Locate the P. falciparum-infected red blood cells and any of indeterminate infection status.
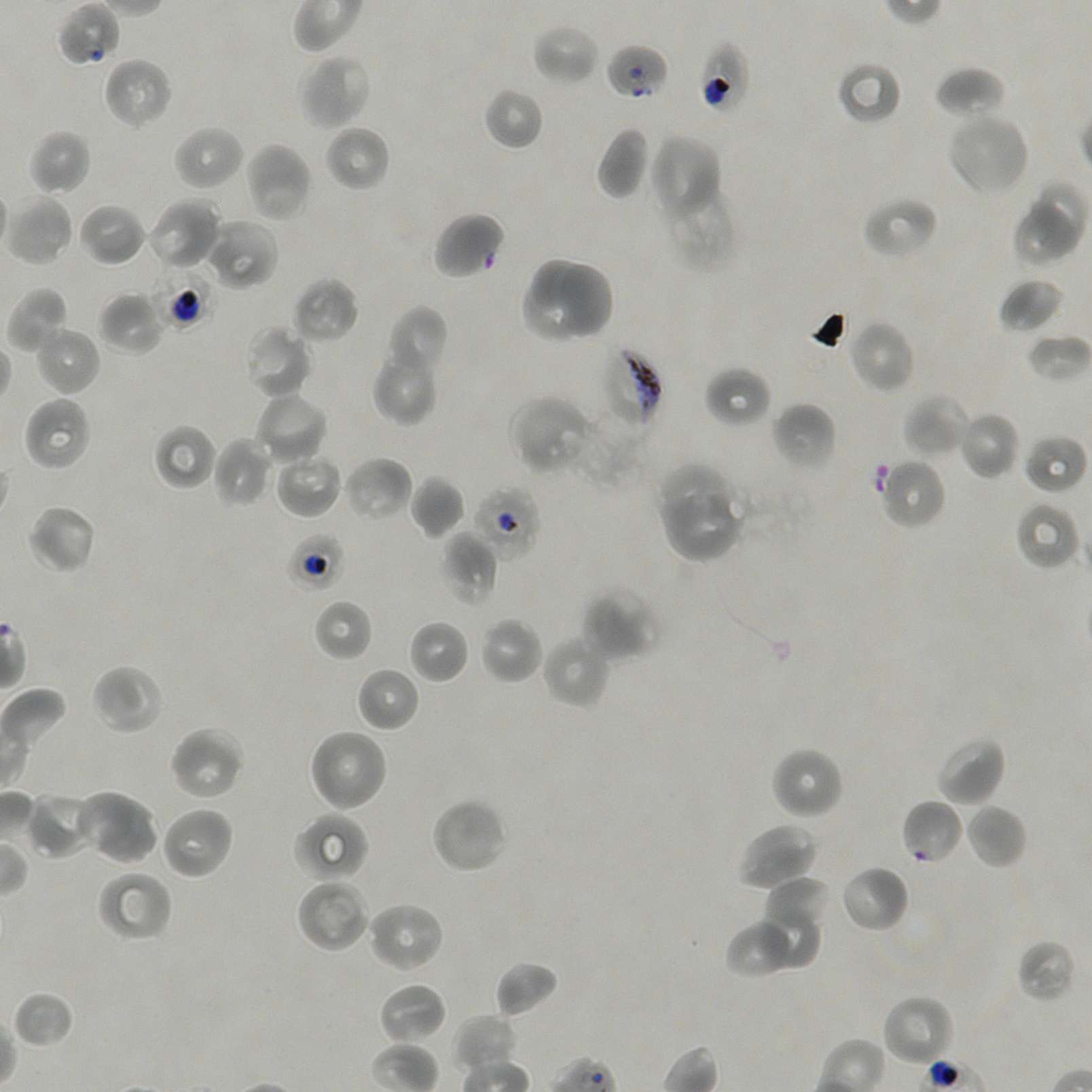

Approximate bounding boxes as {x1, y1, x2, y2} in pixels. Not every red blood cell is marked.
Infected red blood cells: {600, 347, 663, 431}.
Red blood cells of indeterminate infection status: {56, 1, 120, 67}, {697, 41, 751, 115}, {604, 44, 670, 101}, {431, 212, 507, 280}, {156, 267, 211, 328}, {470, 484, 543, 562}, {286, 533, 344, 593}, {901, 798, 964, 864}.

{
  "locations_of_uninfected_red_blood_cells": "{532, 24, 600, 86}, {299, 54, 372, 130}, {102, 57, 174, 130}, {835, 59, 903, 126}, {934, 67, 1006, 120}, {484, 86, 545, 150}, {945, 111, 1030, 197}, {172, 124, 245, 191}, {325, 125, 391, 192}, {596, 126, 650, 199}, {29, 130, 92, 196}, {649, 134, 722, 221}, {244, 141, 313, 223}, {662, 184, 739, 273}, {1025, 184, 1087, 255}, {5, 194, 75, 267}, {862, 195, 939, 260}, {147, 196, 223, 272}, {77, 202, 147, 267}, {1011, 206, 1073, 268}, {203, 218, 279, 291}, {560, 257, 614, 340}, {531, 259, 586, 310}, {291, 276, 359, 345}, {998, 277, 1064, 334}, {522, 282, 587, 341}, {5, 286, 70, 355}, {97, 291, 165, 356}, {386, 305, 449, 378}, {848, 319, 916, 393}, {33, 324, 101, 397}, {244, 324, 314, 401}, {1026, 332, 1091, 384}, {371, 346, 439, 426}, {704, 365, 771, 429}, {253, 390, 329, 465}, {904, 393, 971, 458}, {509, 394, 593, 475}, {22, 395, 93, 472}, {771, 401, 836, 472}, {568, 408, 647, 487}, {958, 410, 1021, 480}, {153, 424, 217, 491}, {1024, 433, 1087, 496}, {211, 437, 273, 509}, {272, 449, 343, 520}, {342, 455, 413, 523}, {878, 457, 947, 530}, {653, 463, 731, 532}, {408, 475, 465, 539}, {664, 494, 744, 562}, {1013, 501, 1081, 571}, {27, 503, 98, 575}, {441, 532, 498, 606}, {580, 585, 658, 662}, {312, 598, 374, 662}, {479, 616, 543, 685}, {407, 619, 470, 685}, {541, 633, 613, 709}, {90, 663, 165, 735}, {356, 667, 420, 733}, {168, 726, 247, 801}, {307, 728, 388, 812}, {934, 735, 1007, 807}, {769, 745, 845, 820}, {75, 788, 159, 866}, {28, 793, 98, 860}, {430, 797, 508, 875}, {965, 803, 1027, 869}, {160, 805, 234, 881}, {293, 812, 369, 881}, {737, 821, 820, 892}, {839, 864, 909, 933}, {96, 871, 172, 943}, {295, 877, 371, 953}, {763, 877, 833, 938}, {367, 901, 445, 973}, {755, 903, 817, 970}, {725, 918, 799, 979}, {1015, 939, 1077, 1004}, {494, 961, 560, 1018}, {378, 983, 448, 1045}, {12, 990, 75, 1049}, {881, 993, 956, 1068}, {451, 1014, 519, 1072}",
  "field_of_view": "single",
  "stain": "Giemsa",
  "donor_blood_group": "A+/O+",
  "preparation": "thin blood film",
  "objective": "100x, oil immersion, numerical aperture 1.45",
  "image_size": "1092×1092 pixels",
  "culture": "in-vitro P. falciparum strain NF54, static"
}